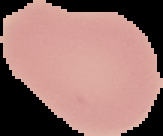
Image is 163×136 pixels. Result: no malaria parasites seen. From a thin blood smear. Segmented cell region on a black background.